Point out every malaria parasite and every leukocyte.
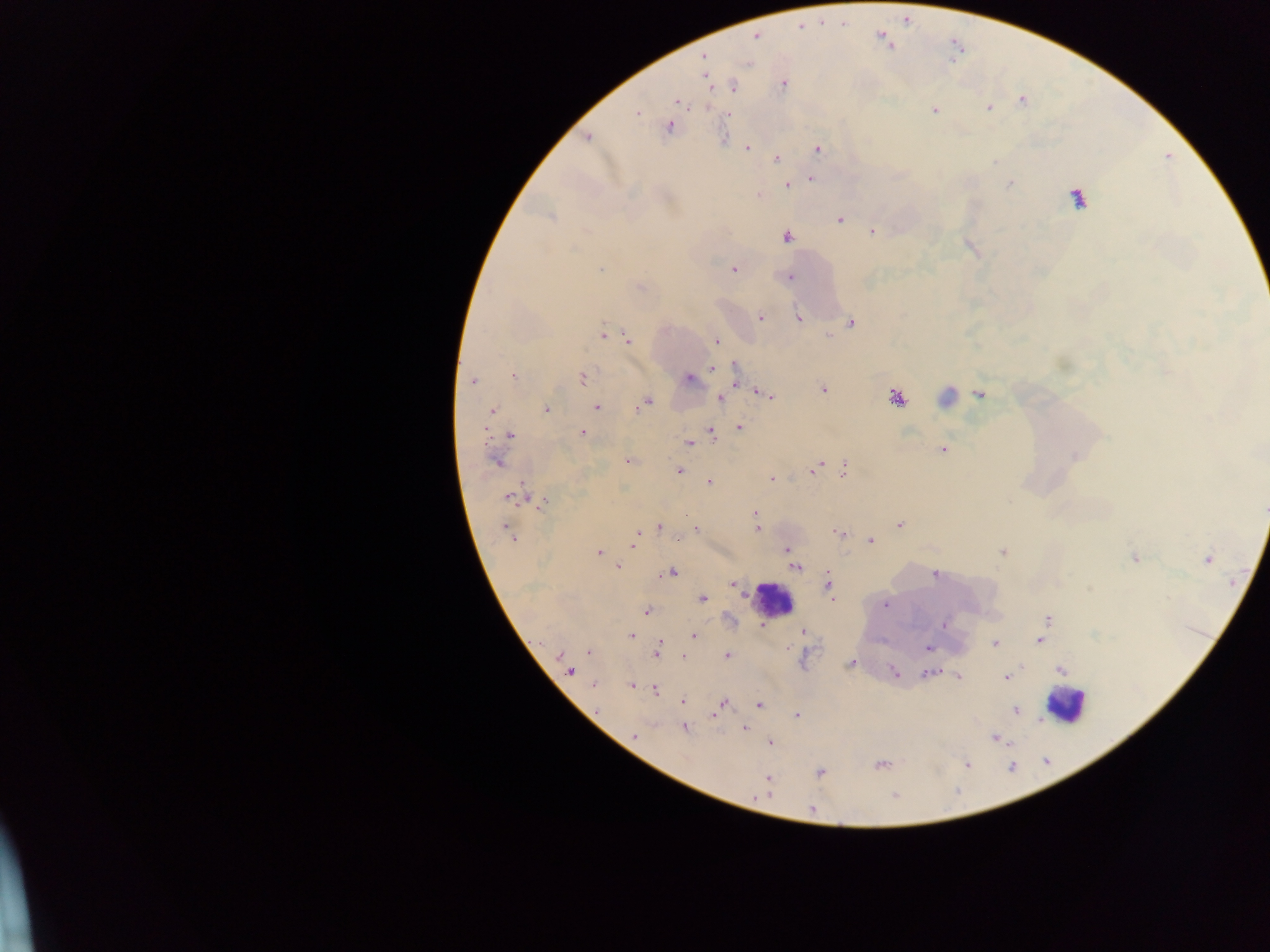
Approximate centers as [x, y] in pixels.
Malaria parasites: [756, 35], [704, 57], [706, 78], [783, 84], [733, 87], [676, 101], [1022, 101], [988, 108], [934, 110], [637, 113], [727, 114], [669, 127], [587, 138], [747, 148], [817, 149], [777, 159], [811, 179], [1009, 184], [787, 185], [759, 196], [1077, 198], [550, 217], [839, 219], [872, 231], [787, 237], [601, 269], [733, 269], [790, 277], [639, 287], [761, 318], [799, 319], [852, 323], [603, 335], [829, 336], [627, 338], [716, 342], [712, 368], [735, 368], [514, 375], [583, 378], [689, 379], [736, 380], [473, 381], [823, 389], [762, 394], [979, 394], [768, 395], [720, 398], [896, 398], [647, 401], [597, 407], [547, 410], [492, 411], [739, 427], [485, 430], [582, 432], [711, 433], [510, 435], [689, 443], [943, 449], [495, 461], [627, 461], [814, 469], [843, 469], [679, 471], [771, 478], [709, 481], [509, 498], [542, 505], [1264, 509], [755, 513], [900, 525], [659, 527], [696, 529], [756, 529], [508, 532], [839, 532], [512, 537], [677, 539], [871, 541], [633, 544], [787, 549], [1002, 552], [597, 553], [1135, 558], [1208, 559], [618, 567], [796, 567], [670, 573], [935, 574], [829, 584], [735, 586], [832, 598], [703, 600], [885, 604], [646, 611], [1045, 621], [944, 625], [763, 626], [803, 631], [631, 636], [694, 636], [660, 639], [1040, 640], [994, 643], [928, 648], [589, 652], [560, 654], [657, 654], [727, 655], [683, 656], [850, 664], [1060, 670], [893, 671], [570, 672], [928, 673], [957, 676], [1007, 677], [594, 685], [631, 686], [655, 690], [683, 701], [721, 704], [759, 705], [719, 708], [1015, 710], [714, 714], [796, 715], [745, 728], [684, 729], [634, 736], [994, 739], [770, 742], [967, 764], [881, 765], [821, 773], [767, 778], [894, 796], [811, 809].
Leukocytes: [946, 396], [772, 599], [1065, 706].

Summary:
  - Country: Ghana
  - Field of view: single
  - Image size: 1270×952 pixels
  - Preparation: thick blood film
  - Capture: mobile-phone photograph through a microscope